Locate every uninfected red blood cell.
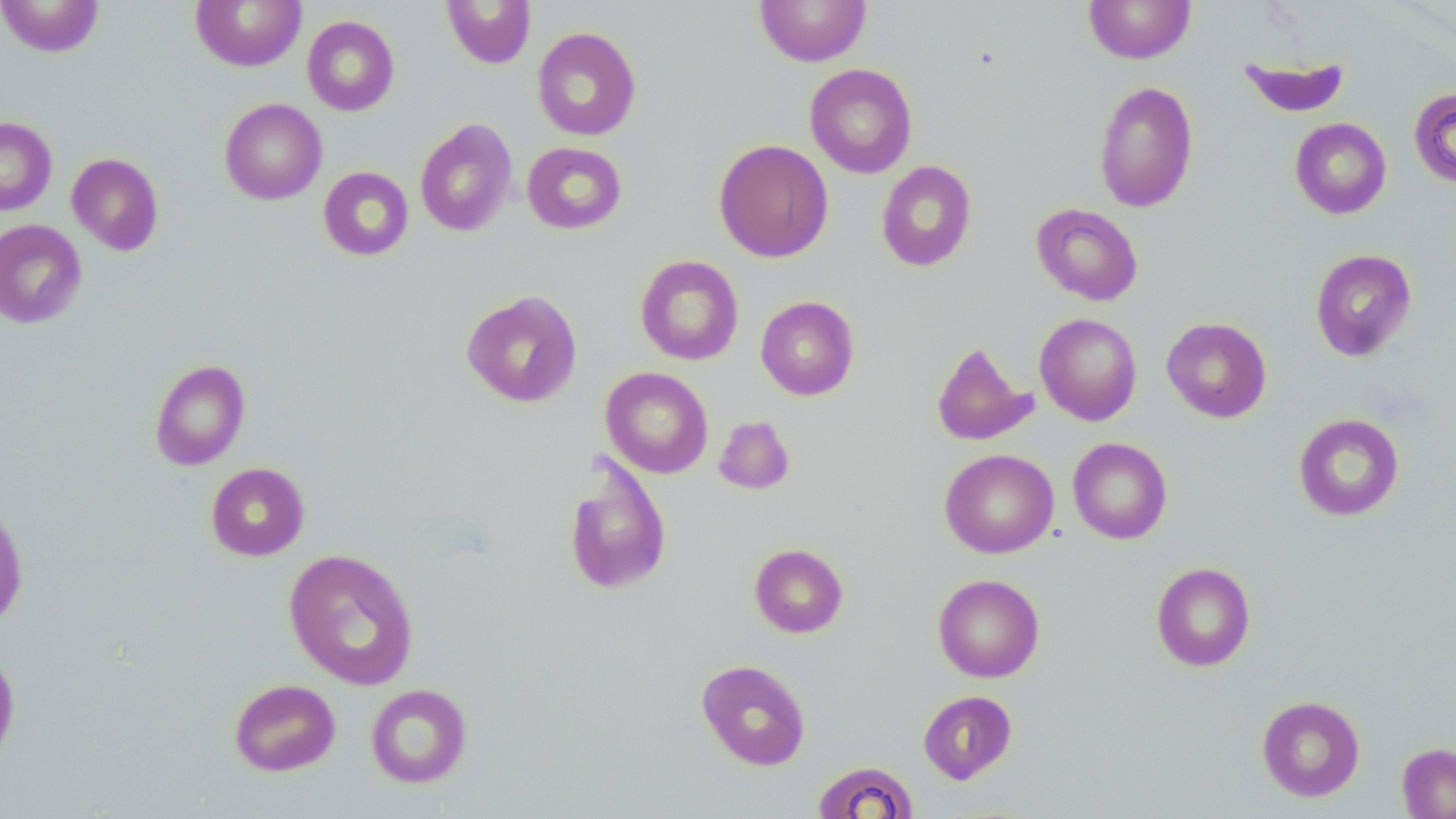

Approximate bounding boxes as (x1,y1)-(x2,y2) corner pairs in pixels.
Uninfected red blood cells: (0,0)-(104,57), (191,0)-(306,72), (441,0)-(536,69), (754,0)-(872,66), (1083,0)-(1196,64), (302,16)-(400,116), (532,27)-(641,141), (1238,55)-(1350,117), (804,63)-(917,178), (1093,80)-(1199,213), (1409,88)-(1456,189), (219,98)-(327,204), (0,117)-(57,215), (1289,117)-(1392,219), (415,118)-(517,237), (713,139)-(834,262), (522,141)-(628,234), (66,152)-(164,256), (876,160)-(977,272), (318,166)-(413,261), (1031,203)-(1143,306), (0,219)-(87,328), (1310,248)-(1417,361), (635,255)-(744,365), (461,289)-(583,407), (756,296)-(859,400), (1035,313)-(1142,426), (1161,317)-(1272,423), (931,340)-(1038,446), (149,359)-(251,471), (600,367)-(713,478), (1293,413)-(1405,522), (713,415)-(796,495), (1068,437)-(1172,544), (940,449)-(1059,558), (562,451)-(673,597), (206,462)-(310,561), (0,498)-(29,630), (749,543)-(848,638), (283,548)-(420,690), (1151,562)-(1256,671), (933,574)-(1045,682), (0,643)-(22,767), (696,659)-(811,771), (228,678)-(340,776), (365,683)-(472,788), (918,690)-(1018,784), (1256,695)-(1365,802), (1397,742)-(1456,818), (812,760)-(920,818).

Slide-level diagnosis: negative for blood parasites. May-Grünwald-Giemsa-stained preparation. Optical microscopy. Captured at 1000x magnification. Thin blood smear. Image is 1456×819 pixels. One field of a larger specimen.